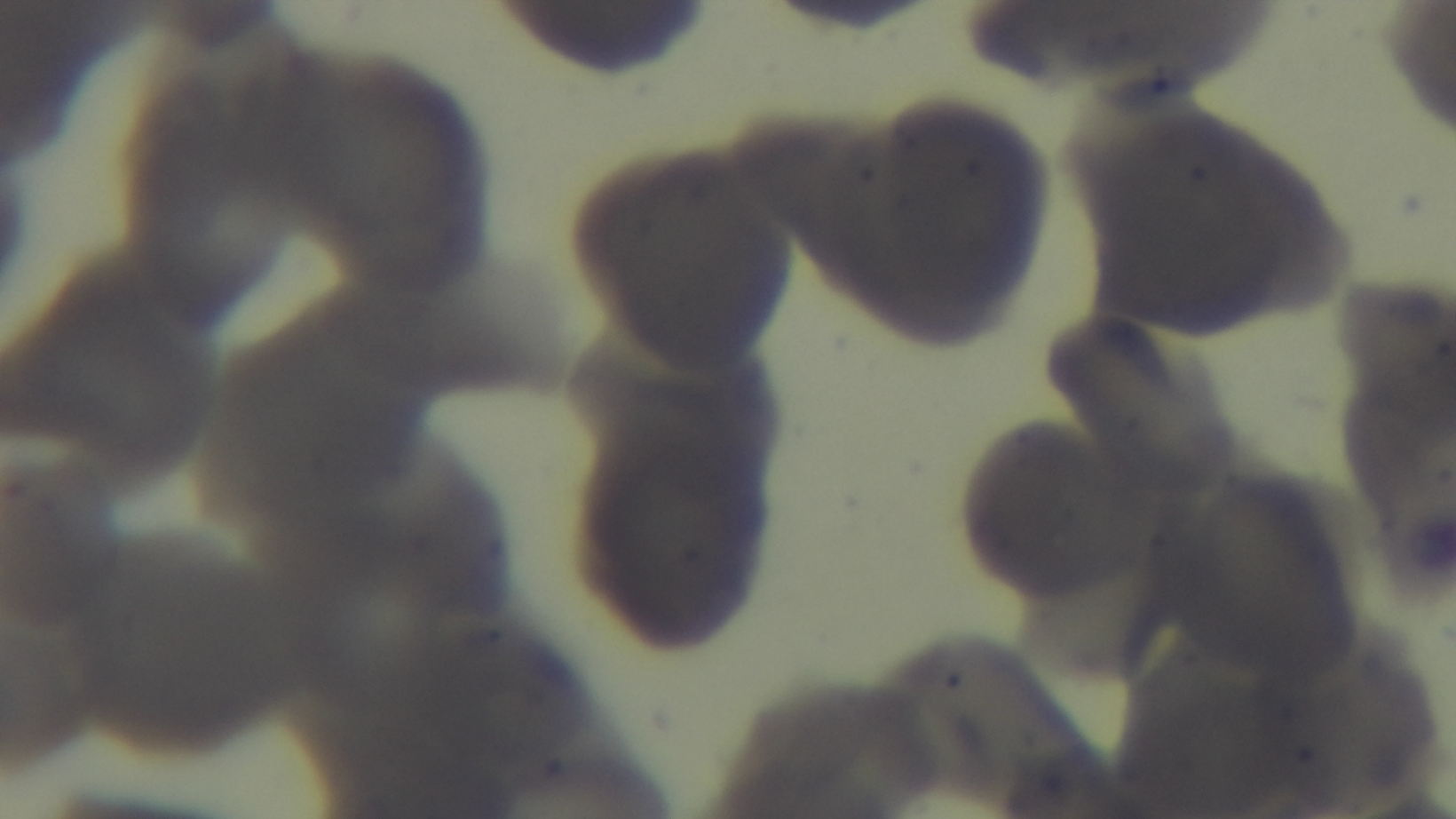
Summary:
  - Modality: light microscopy
  - Preparation: thin
  - Objective: 100x oil immersion
  - Malaria status: negative
  - Stain: Giemsa
  - Capture: mounted 4K digital camera
  - Field of view: one from the slide